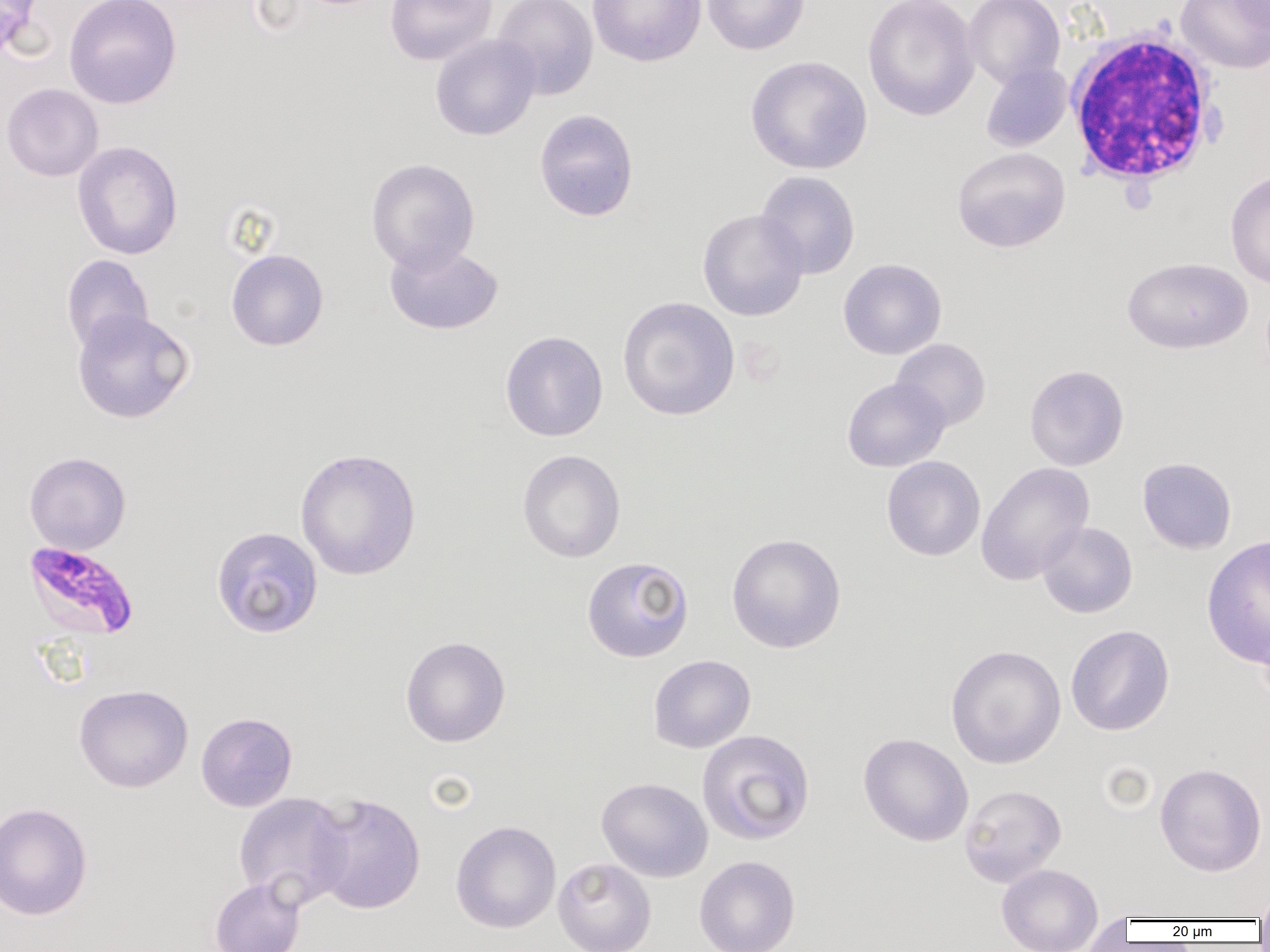 Approximate bounding boxes as named x1/y1/x2/y2 corners in pixels. Plasmodium falciparum-infected red blood cell locations: (x1=21, y1=540, x2=140, y2=640). Uninfected red blood cell locations: (x1=0, y1=0, x2=39, y2=60), (x1=64, y1=0, x2=182, y2=109), (x1=384, y1=0, x2=497, y2=66), (x1=492, y1=0, x2=599, y2=101), (x1=588, y1=0, x2=706, y2=67), (x1=702, y1=0, x2=811, y2=55), (x1=862, y1=0, x2=980, y2=121), (x1=964, y1=0, x2=1065, y2=89), (x1=1176, y1=0, x2=1270, y2=74), (x1=1226, y1=0, x2=1270, y2=33), (x1=430, y1=35, x2=541, y2=141), (x1=745, y1=55, x2=872, y2=174), (x1=980, y1=62, x2=1072, y2=152), (x1=1, y1=83, x2=104, y2=181), (x1=534, y1=108, x2=639, y2=221), (x1=72, y1=141, x2=183, y2=260), (x1=952, y1=147, x2=1071, y2=253), (x1=366, y1=158, x2=480, y2=273), (x1=755, y1=170, x2=860, y2=279), (x1=1225, y1=170, x2=1270, y2=290), (x1=697, y1=209, x2=809, y2=321), (x1=384, y1=241, x2=503, y2=335), (x1=226, y1=248, x2=329, y2=351), (x1=61, y1=255, x2=154, y2=354), (x1=1123, y1=257, x2=1252, y2=354), (x1=838, y1=258, x2=947, y2=360), (x1=617, y1=296, x2=740, y2=421), (x1=72, y1=309, x2=194, y2=424), (x1=500, y1=330, x2=608, y2=441), (x1=891, y1=338, x2=991, y2=431), (x1=1024, y1=364, x2=1129, y2=471), (x1=842, y1=377, x2=950, y2=472), (x1=295, y1=447, x2=421, y2=580), (x1=517, y1=449, x2=626, y2=563), (x1=24, y1=452, x2=131, y2=554), (x1=881, y1=456, x2=985, y2=561), (x1=1137, y1=457, x2=1237, y2=554), (x1=976, y1=462, x2=1095, y2=585), (x1=1036, y1=521, x2=1137, y2=618), (x1=211, y1=526, x2=323, y2=639), (x1=726, y1=533, x2=847, y2=653), (x1=1201, y1=535, x2=1270, y2=668), (x1=581, y1=556, x2=694, y2=662), (x1=1256, y1=612, x2=1270, y2=713), (x1=1065, y1=624, x2=1175, y2=736), (x1=400, y1=636, x2=511, y2=747), (x1=945, y1=644, x2=1066, y2=769), (x1=648, y1=654, x2=756, y2=753), (x1=73, y1=684, x2=193, y2=793), (x1=196, y1=711, x2=297, y2=812), (x1=696, y1=729, x2=815, y2=846), (x1=858, y1=732, x2=974, y2=846), (x1=1155, y1=762, x2=1267, y2=877), (x1=596, y1=777, x2=713, y2=882), (x1=959, y1=784, x2=1066, y2=887), (x1=233, y1=792, x2=352, y2=909), (x1=308, y1=792, x2=426, y2=914), (x1=0, y1=802, x2=93, y2=920), (x1=451, y1=820, x2=561, y2=933), (x1=694, y1=855, x2=800, y2=952), (x1=553, y1=857, x2=656, y2=952), (x1=997, y1=863, x2=1103, y2=952), (x1=209, y1=876, x2=305, y2=952), (x1=1254, y1=885, x2=1270, y2=923), (x1=1078, y1=912, x2=1133, y2=951). White blood cell locations: (x1=1064, y1=27, x2=1224, y2=188). Slide-level diagnosis: Plasmodium falciparum. Single field of view. Captured at 1000x magnification. Optical microscopy. Thin blood film. Image is 1270×952 pixels.